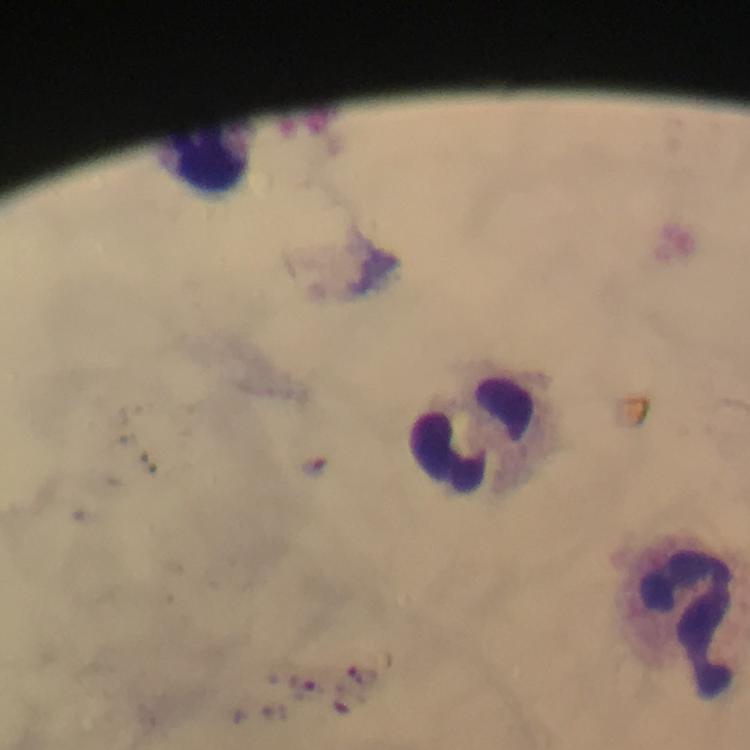
{
  "capture": "smartphone photograph through a microscope",
  "cropped_from": "one field of view",
  "image_size": "750×750 pixels",
  "plasmodium_parasite_locations": "approximate centers as {x, y} in pixels: {305, 684}",
  "leukocyte_locations": "approximate centers as {x, y} in pixels: {210, 160}, {470, 437}, {686, 619}",
  "immersion_oil": "used",
  "stain": "Giemsa",
  "context": "from a malaria diagnostic workup",
  "preparation": "thick smear",
  "magnification": "100x"
}